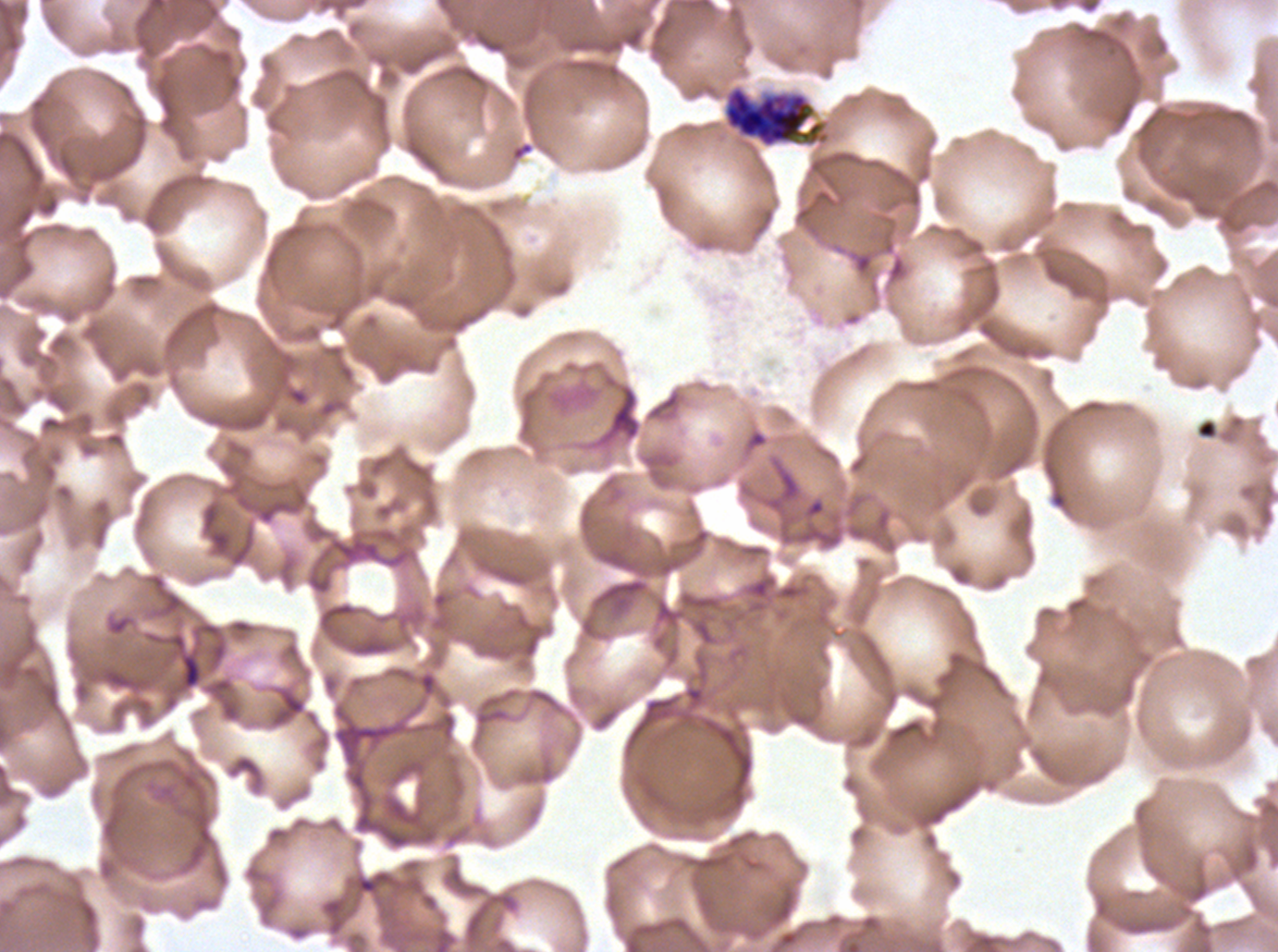
notation = approximate bounding boxes as [x1, y1, x2, y2] in pixels
debris locations = [1196, 418, 1218, 440]
late schizont locations = [721, 83, 831, 149]
field of view = sub-image separated from a larger composite
specimen = P. falciparum from a patient in The Gambia, cultured ex vivo for 24 to 48 hours
image size = 1278×952 pixels
preparation = thin blood film
stain = Giemsa